Report the malaria status.
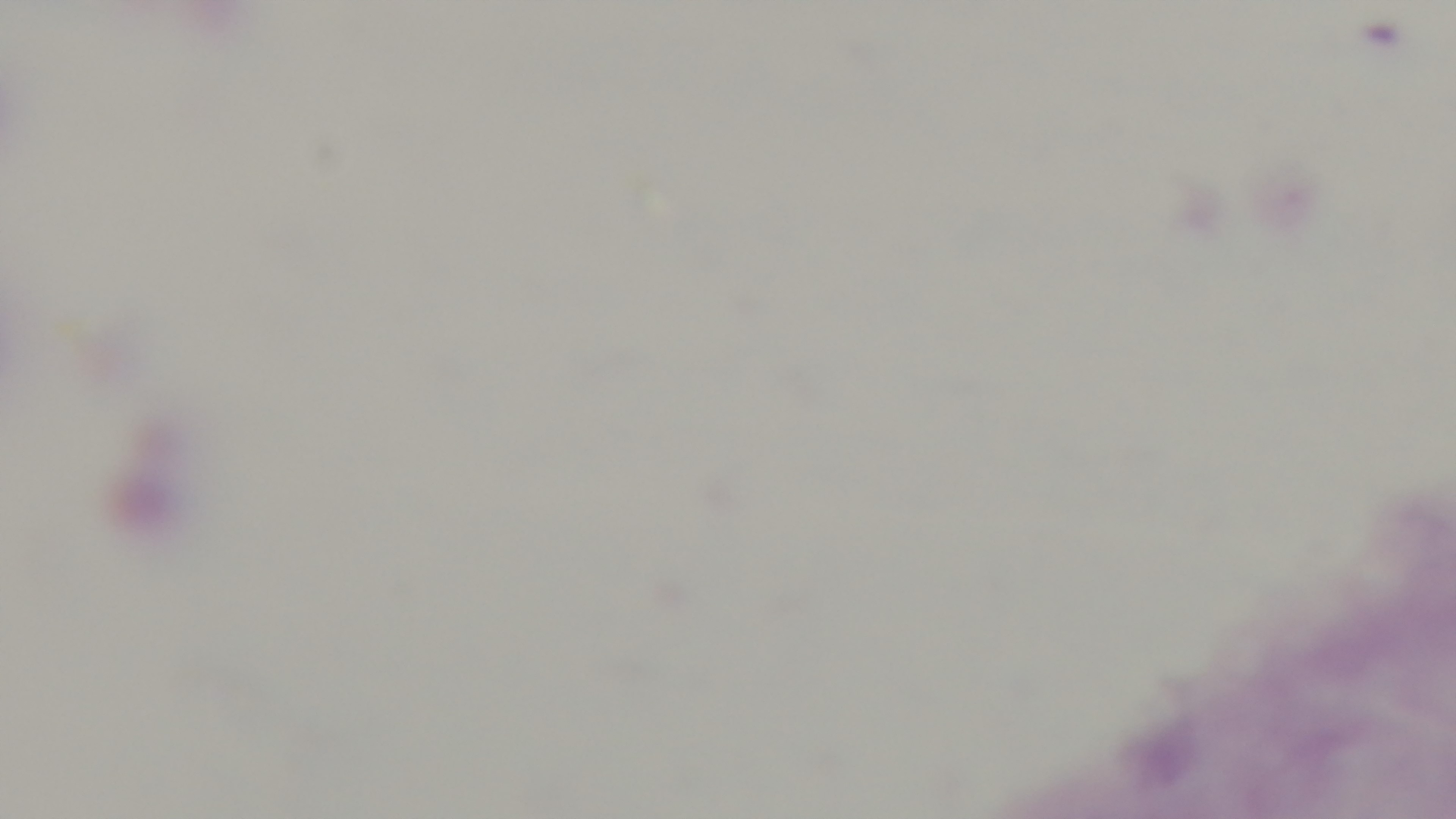

It is uninfected.

Light microscopy. Giemsa stain. Preparation: thick. Mounted 4K digital camera. Single field of view. 100x oil-immersion objective.